Name the parasite shown.
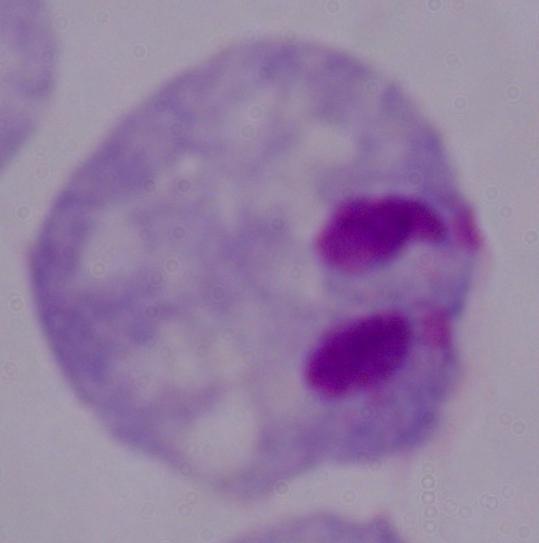
A trichomonad.

Photomicrograph. Captured at 1000x magnification.